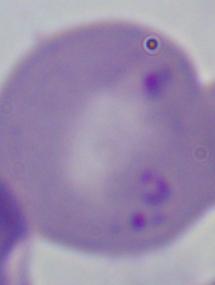

identification: Babesia
magnification: 1000x
modality: micrograph